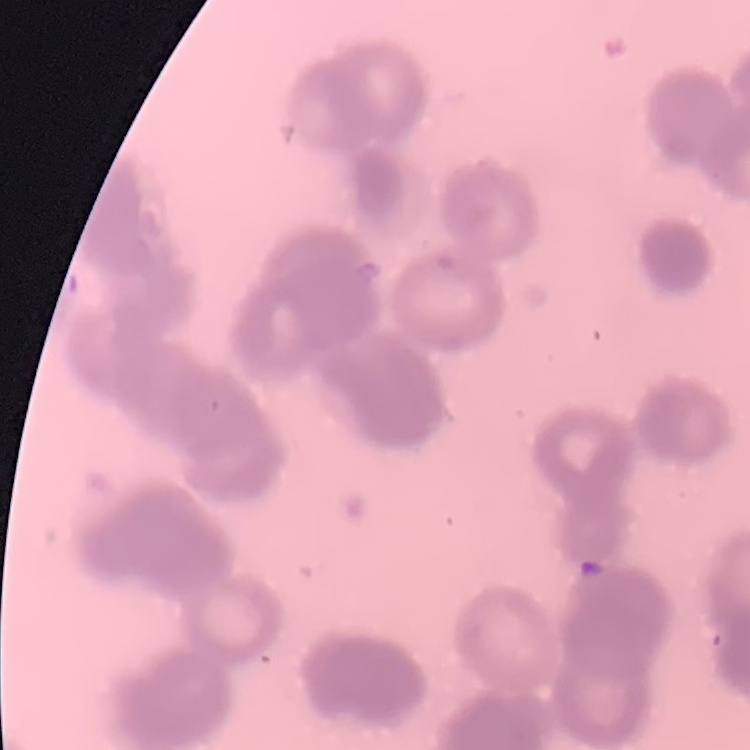
erythrocyte morphology = rouleaux formation
image type = one tile cut from a larger photomicrograph
preparation = thin blood smear
stain = Field's or Giemsa